Identify the blood parasite species.
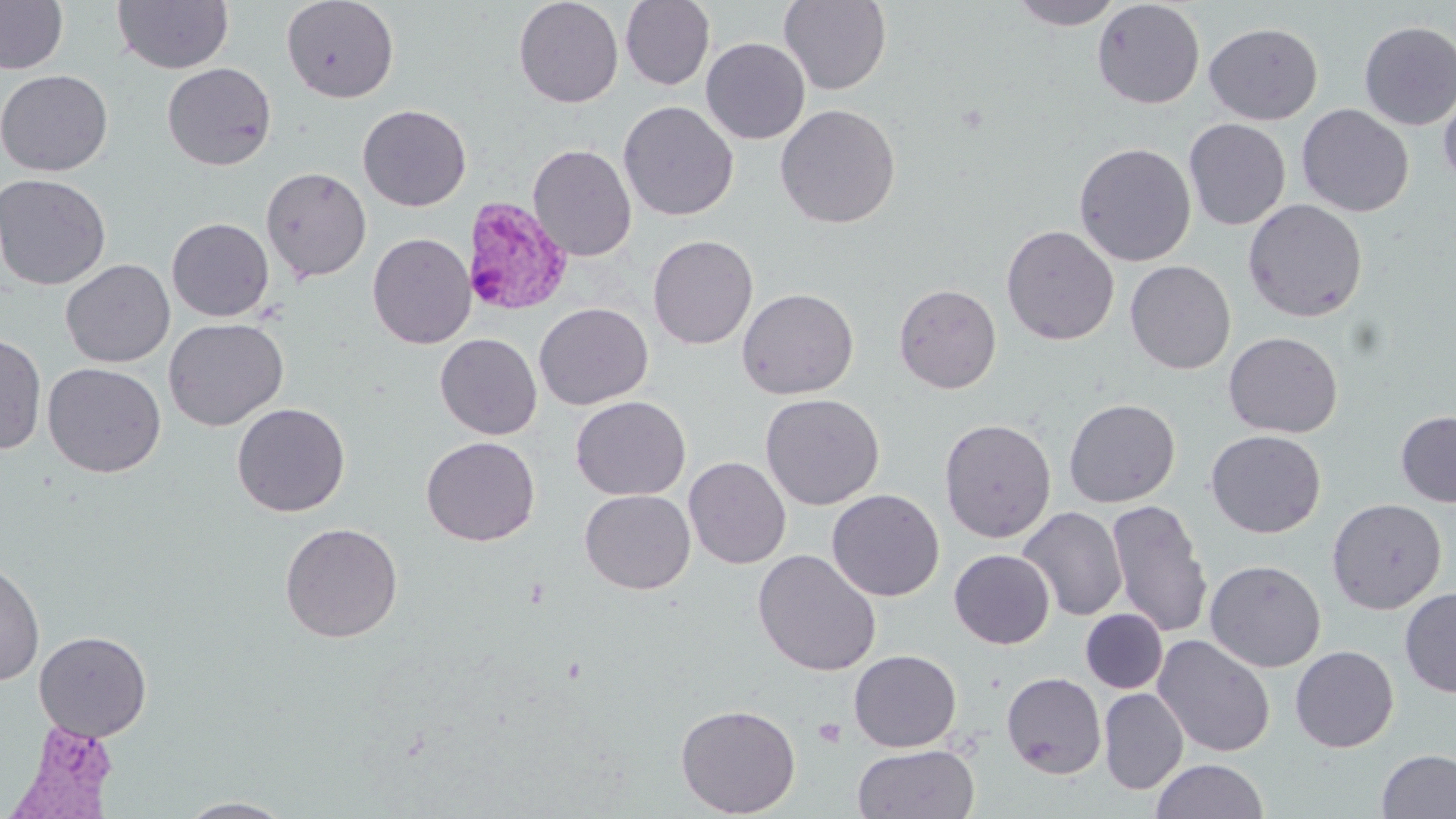

Plasmodium vivax.

Approximate bounding boxes as named x1/y1/x2/y2 corners in pixels. Plasmodium vivax-infected red blood cell locations: (x1=462, y1=197, x2=574, y2=318), (x1=5, y1=725, x2=127, y2=818). Platelet locations: (x1=813, y1=717, x2=847, y2=748). Uninfected red blood cell locations: (x1=0, y1=0, x2=69, y2=74), (x1=112, y1=0, x2=234, y2=74), (x1=281, y1=0, x2=399, y2=103), (x1=514, y1=0, x2=623, y2=108), (x1=620, y1=0, x2=715, y2=90), (x1=778, y1=0, x2=892, y2=95), (x1=1008, y1=0, x2=1125, y2=29), (x1=1092, y1=1, x2=1205, y2=109), (x1=1092, y1=12, x2=1324, y2=113), (x1=1358, y1=21, x2=1456, y2=130), (x1=1203, y1=22, x2=1323, y2=125), (x1=701, y1=37, x2=810, y2=144), (x1=162, y1=62, x2=277, y2=171), (x1=0, y1=69, x2=114, y2=176), (x1=1439, y1=85, x2=1456, y2=193), (x1=618, y1=101, x2=738, y2=221), (x1=357, y1=104, x2=472, y2=212), (x1=775, y1=104, x2=900, y2=228), (x1=1297, y1=104, x2=1414, y2=217), (x1=1183, y1=119, x2=1291, y2=230), (x1=1073, y1=142, x2=1196, y2=267), (x1=528, y1=143, x2=637, y2=262), (x1=261, y1=166, x2=372, y2=283), (x1=0, y1=172, x2=111, y2=290), (x1=1243, y1=199, x2=1368, y2=322), (x1=167, y1=217, x2=274, y2=321), (x1=1001, y1=225, x2=1119, y2=346), (x1=367, y1=232, x2=476, y2=349), (x1=647, y1=234, x2=758, y2=350), (x1=60, y1=258, x2=175, y2=367), (x1=1125, y1=260, x2=1236, y2=374), (x1=894, y1=283, x2=1002, y2=394), (x1=737, y1=288, x2=859, y2=399), (x1=534, y1=302, x2=653, y2=410), (x1=163, y1=318, x2=288, y2=431), (x1=0, y1=332, x2=47, y2=455), (x1=1223, y1=332, x2=1343, y2=438), (x1=435, y1=333, x2=542, y2=439), (x1=43, y1=362, x2=166, y2=478), (x1=760, y1=393, x2=884, y2=510), (x1=571, y1=396, x2=691, y2=501), (x1=1063, y1=398, x2=1180, y2=507), (x1=231, y1=402, x2=350, y2=517), (x1=1396, y1=411, x2=1456, y2=507), (x1=939, y1=418, x2=1057, y2=543), (x1=1206, y1=430, x2=1325, y2=538), (x1=421, y1=436, x2=541, y2=546), (x1=684, y1=456, x2=791, y2=569), (x1=579, y1=489, x2=695, y2=594), (x1=827, y1=489, x2=944, y2=601), (x1=1327, y1=498, x2=1447, y2=614), (x1=1107, y1=500, x2=1213, y2=639), (x1=1017, y1=506, x2=1127, y2=621), (x1=280, y1=522, x2=403, y2=643), (x1=753, y1=549, x2=881, y2=676), (x1=949, y1=549, x2=1055, y2=649), (x1=0, y1=558, x2=45, y2=687), (x1=1205, y1=560, x2=1326, y2=672), (x1=1400, y1=588, x2=1456, y2=698), (x1=1081, y1=609, x2=1168, y2=693), (x1=34, y1=630, x2=152, y2=741), (x1=1153, y1=634, x2=1275, y2=757), (x1=1290, y1=645, x2=1399, y2=752), (x1=848, y1=649, x2=961, y2=752), (x1=1001, y1=672, x2=1106, y2=779), (x1=1099, y1=688, x2=1188, y2=795), (x1=675, y1=703, x2=801, y2=817), (x1=852, y1=745, x2=980, y2=819), (x1=1376, y1=749, x2=1456, y2=818), (x1=1149, y1=759, x2=1269, y2=818), (x1=175, y1=797, x2=295, y2=818). Light microscopy. Captured at 1000x magnification. Image is 1456×819 pixels. May-Grünwald-Giemsa-stained preparation. One field of a larger specimen. Thin blood smear.